Describe the morphology of the red blood cells.
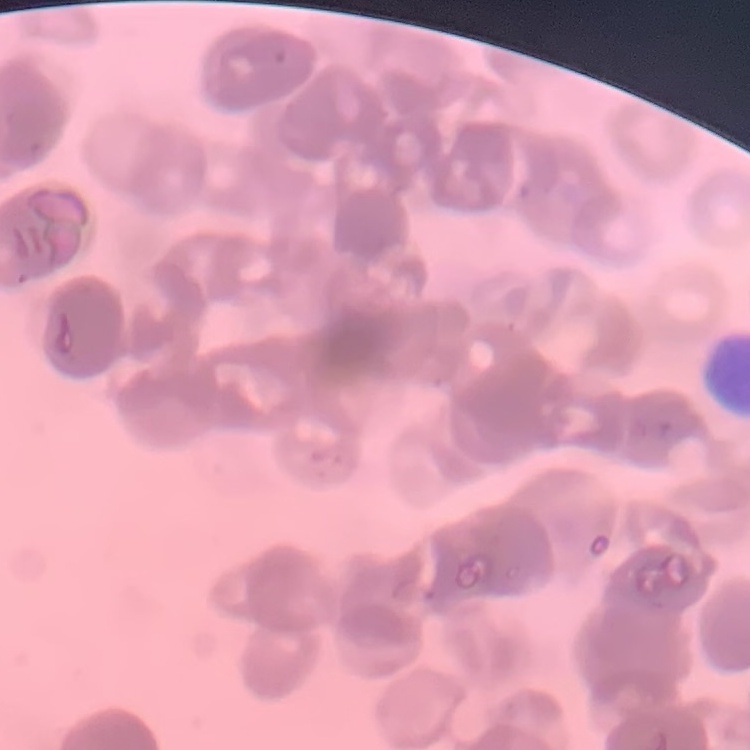

Rouleaux formation.

preparation = thin peripheral smear
image type = square crop of a larger photomicrograph
stain = Field's or Giemsa